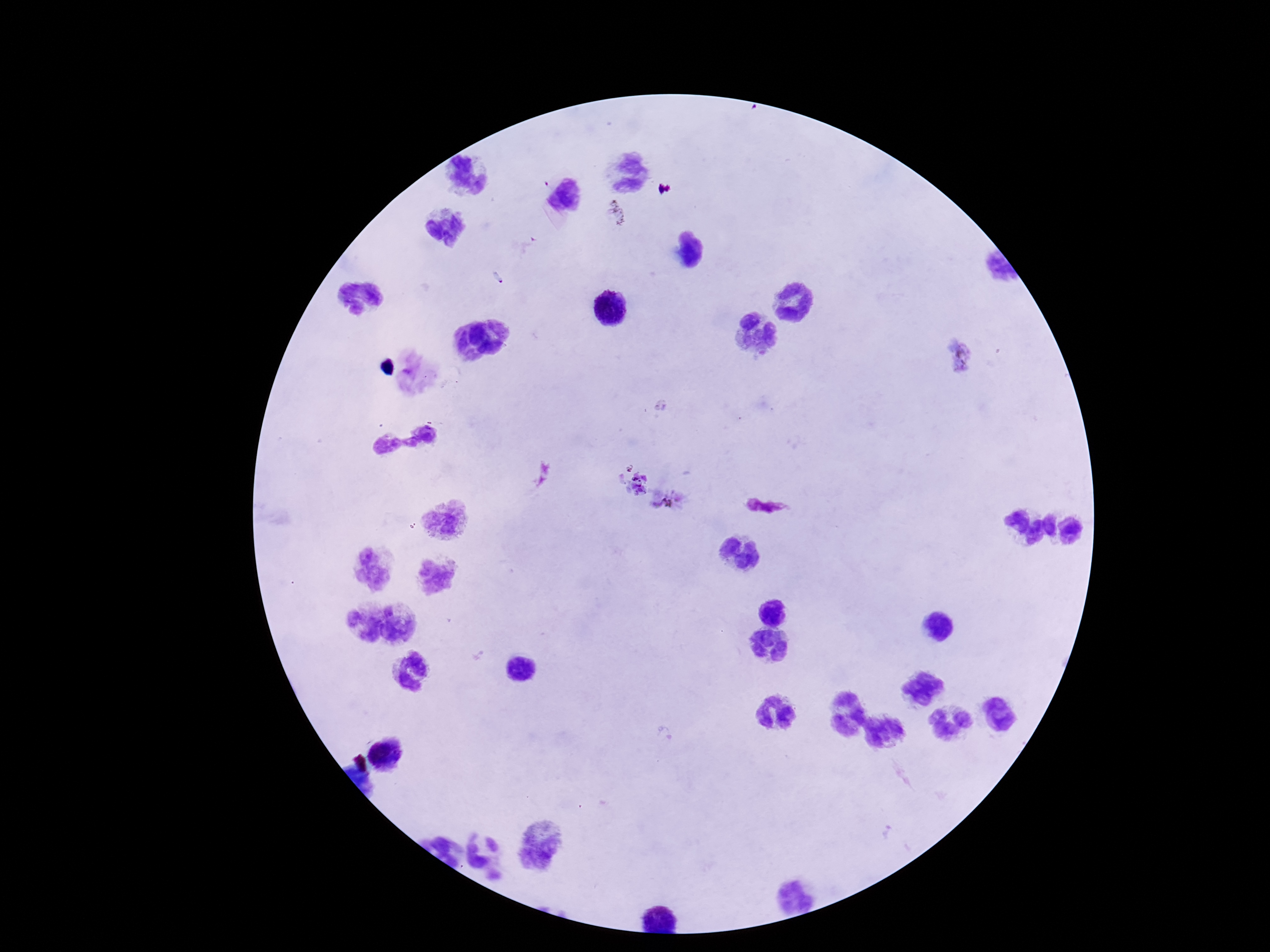
Approximate centers as (x, y) in pixels. Plasmodium parasite locations: (616, 212), (958, 357), (632, 480), (669, 498). Photographed through the microscope eyepiece with a smartphone camera. Patient malaria status: positive. Giemsa-stained preparation. Single field of view. 100x magnification. Thick peripheral-blood smear. Image is 1270×952 pixels.